Assess this cell for malaria.
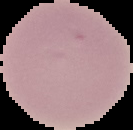

Uninfected.

image_size: 133×130 pixels
preparation: thin blood film
image_type: segmented cell region on a black background